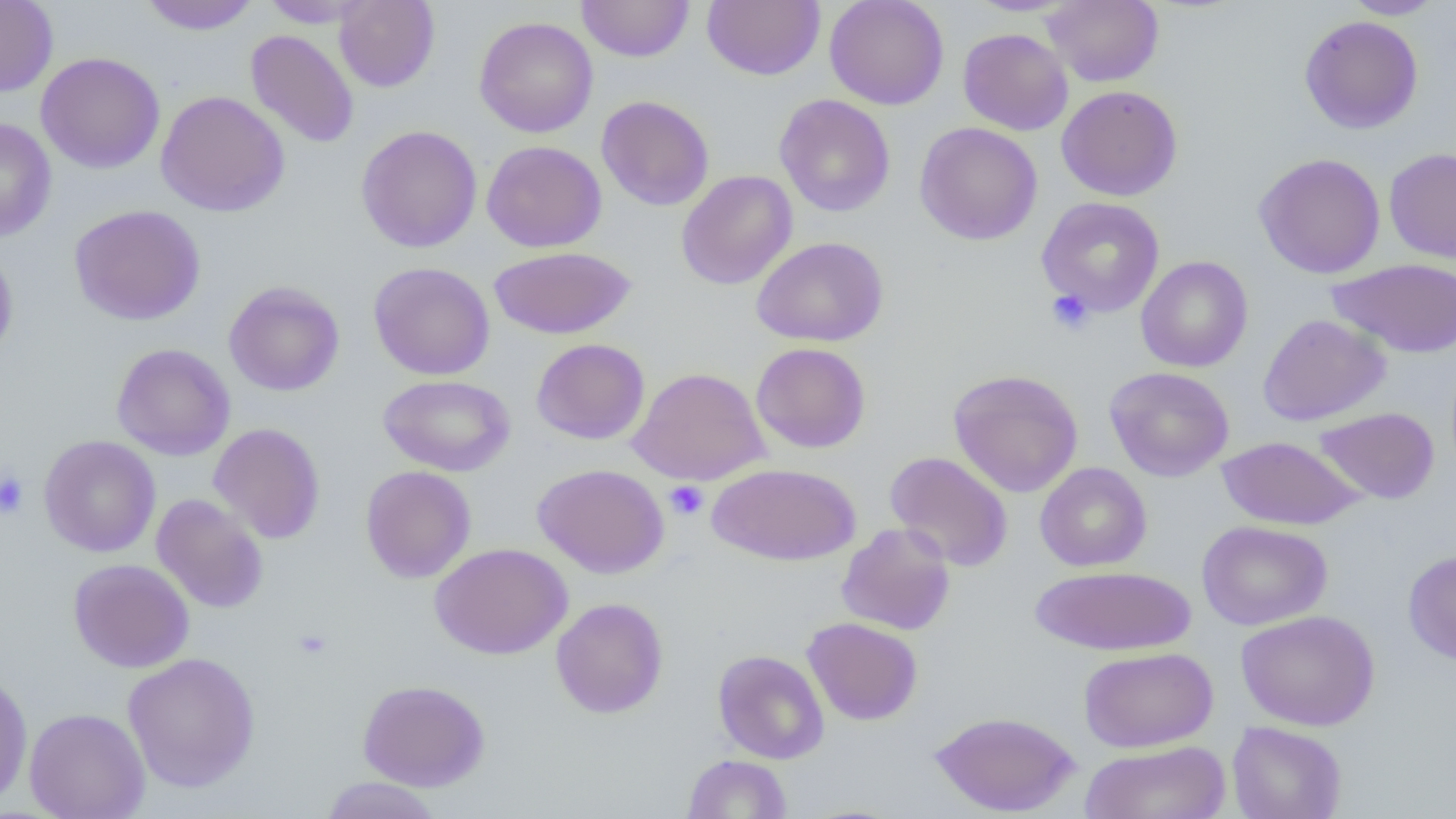
slide-level diagnosis = no evidence of blood parasites
platelet locations = approximate bounding boxes as (x1, y1, x2, y2) in pixels: (1046, 288, 1095, 335), (0, 470, 30, 520), (664, 480, 708, 521), (293, 628, 332, 660)
field of view = single
preparation = thin blood film
image size = 1456×819 pixels
magnification = 1000x
modality = optical microscopy
uninfected red blood cell locations = approximate bounding boxes as (x1, y1, x2, y2) in pixels: (0, 0, 58, 97), (138, 0, 260, 35), (260, 0, 376, 28), (334, 0, 440, 92), (576, 0, 694, 62), (702, 0, 824, 81), (824, 0, 950, 110), (966, 0, 1079, 16), (1043, 0, 1163, 87), (1341, 0, 1446, 19), (1298, 15, 1423, 133), (474, 16, 598, 138), (958, 28, 1073, 135), (245, 29, 359, 149), (36, 52, 165, 174), (1056, 85, 1183, 201), (156, 90, 290, 217), (774, 94, 895, 217), (597, 95, 714, 211), (0, 117, 57, 242), (914, 122, 1043, 245), (356, 125, 483, 253), (481, 140, 607, 252), (1384, 147, 1456, 263), (1254, 152, 1386, 278), (676, 170, 797, 289), (1036, 196, 1165, 316), (69, 204, 206, 325), (751, 236, 889, 347), (0, 241, 19, 365), (488, 245, 636, 340), (1136, 255, 1253, 372), (1327, 257, 1456, 359), (368, 262, 495, 380), (224, 281, 345, 396), (1258, 313, 1391, 425), (532, 338, 650, 445), (750, 342, 871, 453), (111, 343, 235, 461), (628, 366, 769, 485), (1105, 366, 1234, 481), (948, 369, 1084, 497), (378, 374, 516, 476), (1314, 407, 1439, 504), (208, 422, 326, 544), (38, 435, 161, 558), (1217, 435, 1363, 530), (885, 451, 1013, 572), (707, 462, 861, 566), (1035, 462, 1152, 572), (532, 463, 669, 578), (359, 465, 476, 584), (151, 494, 269, 613), (1196, 520, 1332, 630), (836, 522, 956, 635), (429, 542, 572, 659), (1403, 549, 1456, 666), (68, 558, 194, 673), (1031, 565, 1196, 655), (551, 597, 669, 718), (1236, 609, 1380, 731), (802, 617, 923, 725), (1078, 647, 1218, 753), (713, 649, 829, 764), (122, 651, 261, 793), (0, 669, 33, 810), (357, 679, 490, 791), (24, 708, 151, 818), (929, 710, 1082, 816), (1227, 721, 1346, 819), (1079, 740, 1232, 819), (682, 754, 793, 818), (319, 777, 444, 818)